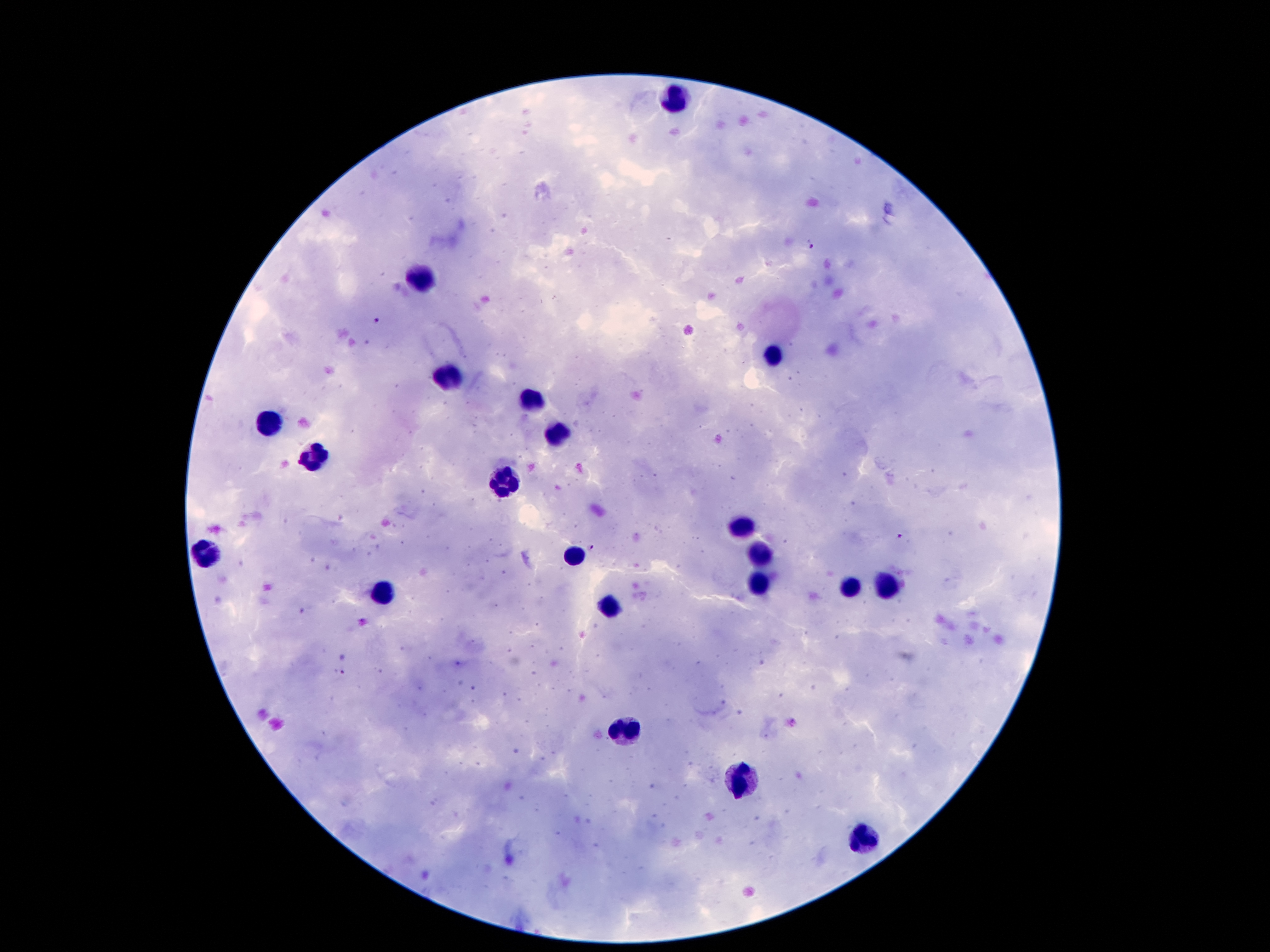

Approximate centers as {x, y} in pixels.
Summary:
  - Leukocyte locations: {676, 98}, {422, 277}, {773, 356}, {447, 377}, {531, 398}, {270, 423}, {556, 432}, {317, 457}, {506, 483}, {739, 529}, {208, 552}, {574, 555}, {760, 557}, {758, 581}, {851, 586}, {887, 586}, {379, 593}, {610, 605}, {630, 729}, {744, 779}, {867, 842}
  - Malaria parasite locations: {810, 244}, {375, 319}, {899, 536}, {590, 546}, {339, 674}
  - Field of view: one from this slide
  - Magnification: 100x
  - Stain: Giemsa
  - Capture: smartphone through the microscope eyepiece
  - Patient malaria status: positive for Plasmodium falciparum
  - Image size: 1270×952 pixels
  - Preparation: thick blood film